Assess for Plasmodium parasites.
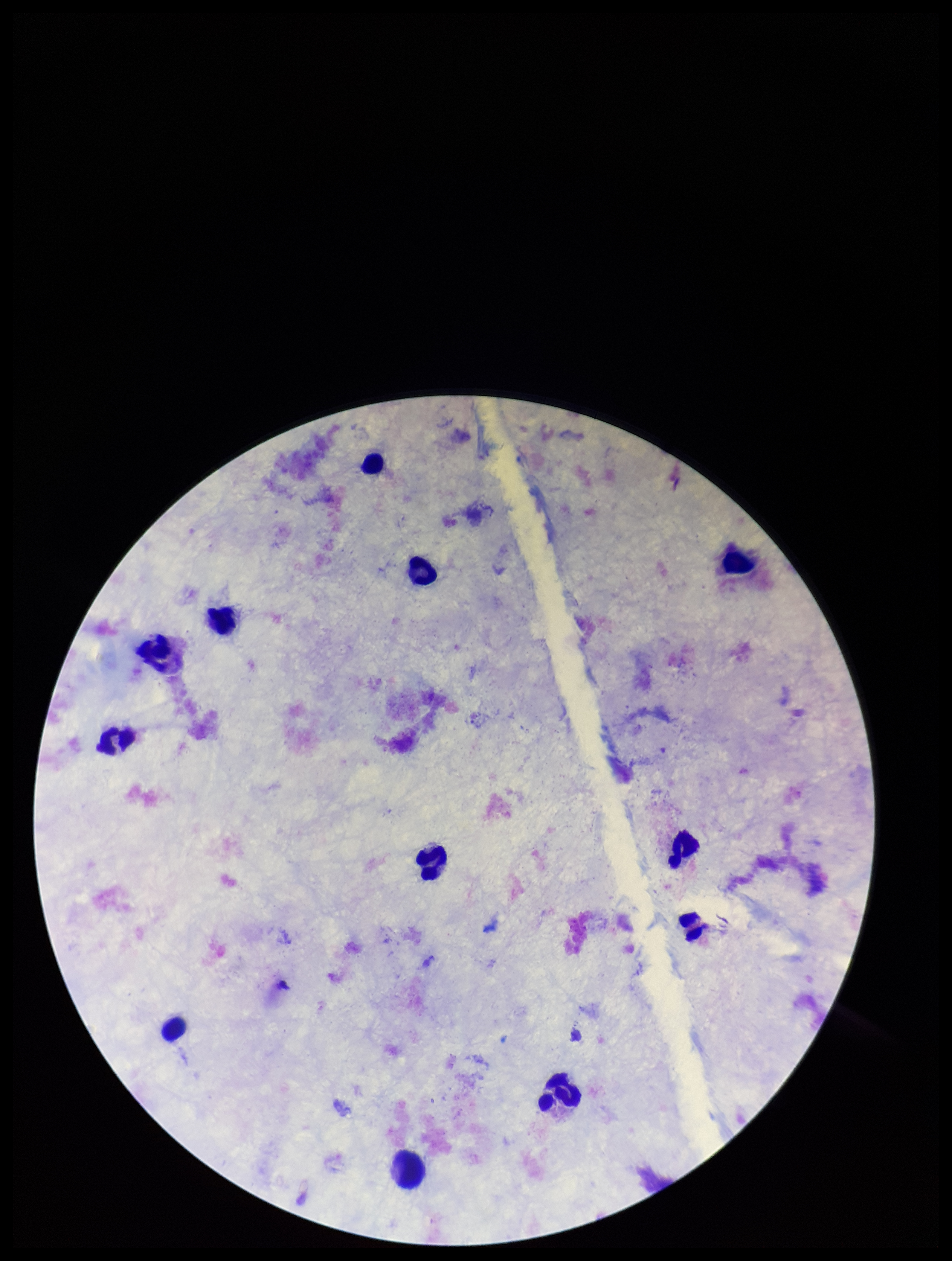

None seen.

Summary:
  - Field of view: one from this slide
  - Patient malaria status: negative
  - Preparation: thick
  - Stain: Giemsa
  - Capture: smartphone photograph through the microscope eyepiece
  - Image size: 952×1261 pixels
  - Parasite count: 0
  - Leukocyte count: 12